State which parasite is depicted.
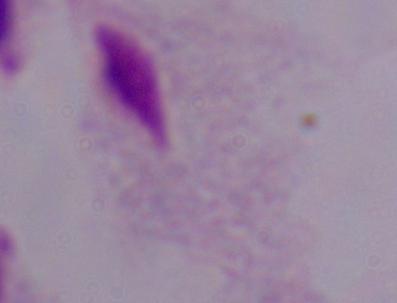
A trichomonad.

magnification = 1000x
modality = photomicrograph